Comment on the morphology of the erythrocytes.
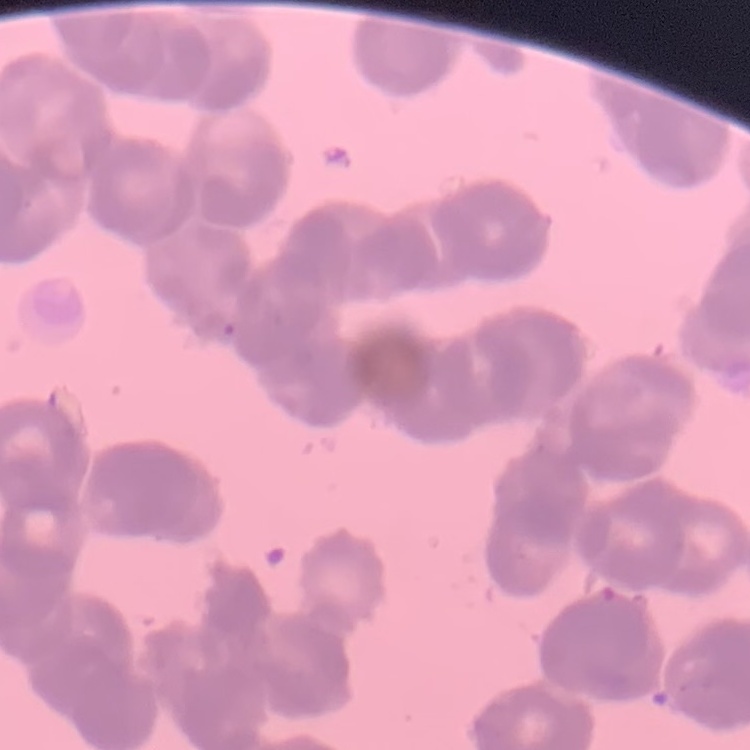

They show rouleaux formation.

Thin peripheral smear. One tile cut from a larger photomicrograph. Stained with either Field's or Giemsa.